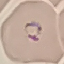

{
  "malaria_status": "parasitized",
  "capture": "smartphone camera at the microscope eyepiece",
  "stain": "Giemsa",
  "image_type": "cell patch, automatically extracted from a larger field of view and resized to 64 × 64 pixels",
  "preparation": "thin blood film"
}